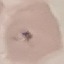
malaria status = uninfected
preparation = thin smear
capture = smartphone camera at the microscope eyepiece
stain = Giemsa
image type = cell patch, automatically extracted from a larger field of view and resized to 64 × 64 pixels